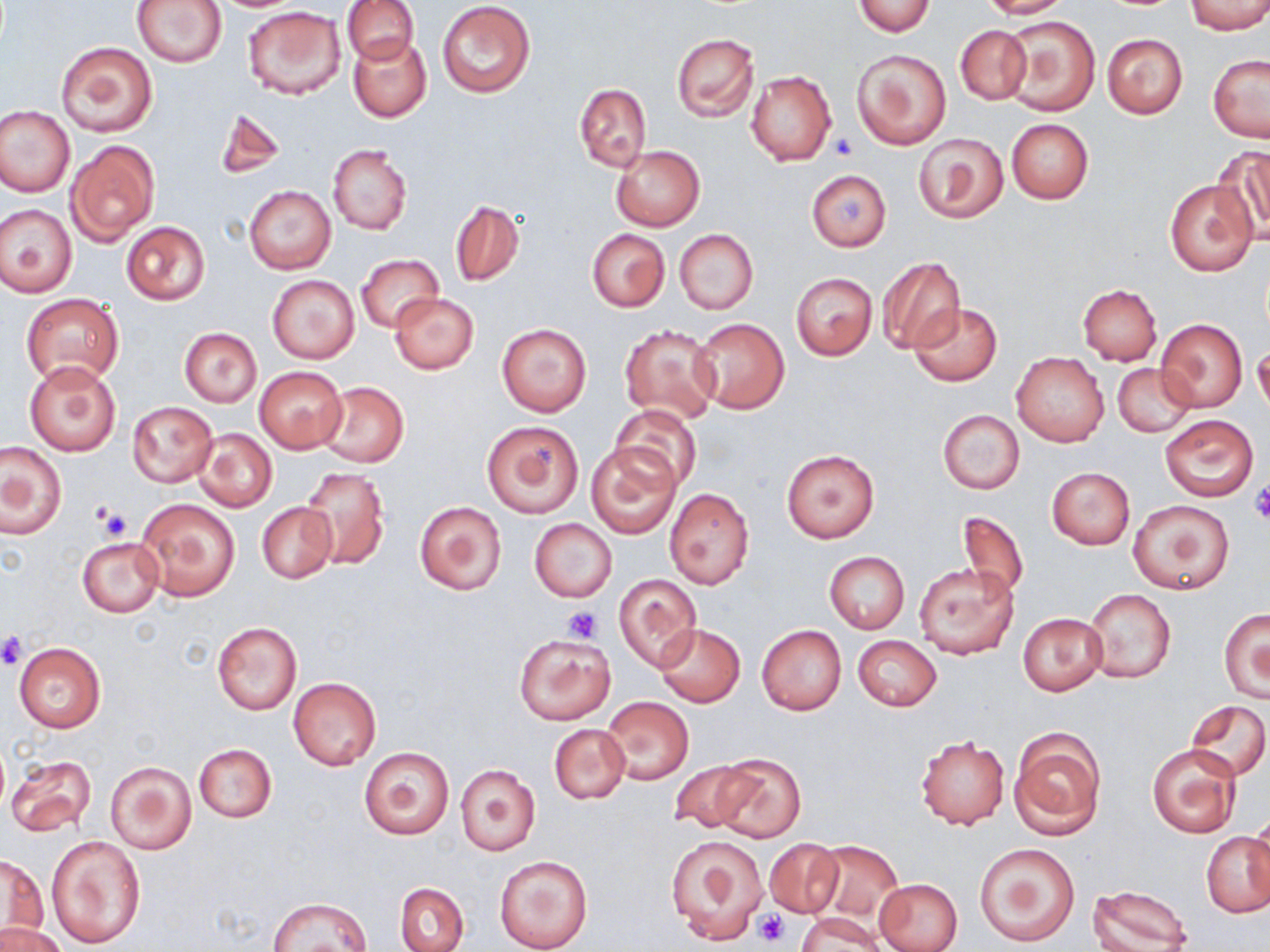 Approximate bounding boxes as [x1, y1, x2, y2] in pixels. Platelet locations: [829, 132, 859, 158], [1249, 482, 1270, 524], [94, 505, 132, 542], [562, 605, 603, 642], [0, 630, 28, 669], [754, 910, 790, 947]. Uninfected red blood cell locations: [131, 0, 228, 68], [342, 0, 419, 64], [977, 0, 1069, 18], [850, 1, 936, 36], [436, 2, 535, 97], [1185, 2, 1270, 34], [243, 7, 346, 99], [1001, 15, 1100, 117], [955, 24, 1030, 103], [672, 33, 758, 122], [1102, 33, 1187, 118], [348, 35, 432, 122], [56, 40, 158, 137], [852, 48, 950, 150], [1208, 55, 1270, 143], [746, 70, 837, 166], [574, 83, 650, 171], [216, 105, 287, 179], [0, 106, 74, 196], [1007, 118, 1093, 204], [914, 132, 1008, 224], [66, 138, 159, 244], [611, 144, 705, 231], [328, 145, 412, 234], [1217, 146, 1270, 242], [806, 169, 891, 251], [1165, 177, 1259, 277], [244, 184, 335, 275], [451, 200, 524, 286], [0, 204, 77, 296], [121, 220, 210, 305], [674, 228, 758, 314], [588, 229, 669, 312], [357, 254, 443, 334], [876, 257, 964, 353], [791, 273, 877, 359], [267, 274, 360, 365], [1078, 283, 1162, 365], [20, 292, 123, 384], [389, 292, 478, 374], [908, 302, 1003, 386], [689, 319, 788, 414], [1155, 319, 1248, 412], [496, 322, 592, 417], [619, 324, 720, 424], [180, 328, 261, 406], [1253, 345, 1270, 419], [1012, 352, 1109, 447], [24, 360, 121, 456], [1112, 363, 1196, 437], [253, 367, 347, 453], [318, 381, 410, 468], [127, 402, 218, 486], [610, 404, 701, 490], [938, 409, 1024, 494], [1161, 415, 1259, 499], [482, 420, 583, 517], [194, 428, 277, 512], [1, 442, 67, 537], [586, 442, 682, 538], [781, 449, 878, 543], [300, 467, 389, 570], [1047, 467, 1135, 548], [663, 487, 754, 588], [136, 498, 240, 601], [414, 500, 508, 596], [1128, 500, 1234, 594], [257, 501, 337, 583], [955, 511, 1028, 602], [529, 518, 617, 603], [77, 537, 165, 616], [825, 551, 909, 634], [914, 562, 1019, 661], [613, 574, 702, 670], [1084, 589, 1176, 682], [1219, 609, 1270, 703], [1018, 613, 1106, 695], [212, 621, 302, 714], [655, 624, 745, 706], [756, 624, 846, 715], [515, 634, 615, 724], [852, 635, 942, 710], [13, 641, 107, 732], [289, 678, 381, 771], [601, 696, 693, 786], [1186, 700, 1270, 782], [549, 724, 629, 802], [1007, 727, 1106, 842], [915, 735, 1009, 831], [194, 743, 276, 823], [1147, 744, 1241, 838], [358, 747, 456, 841], [5, 754, 95, 836], [711, 754, 805, 841], [666, 758, 762, 834], [104, 760, 197, 855], [455, 763, 540, 856], [1246, 816, 1270, 898], [1203, 831, 1270, 918], [665, 833, 768, 945], [46, 836, 145, 949], [765, 838, 841, 916], [811, 840, 902, 925], [974, 841, 1080, 947], [2, 855, 51, 940], [495, 855, 592, 952], [873, 878, 963, 952], [397, 883, 469, 952], [1087, 886, 1195, 952], [267, 896, 373, 950], [796, 913, 883, 952], [0, 924, 66, 952]. Slide-level diagnosis: negative for blood parasites. One field of a larger specimen. Light microscopy. Image is 1270×952 pixels. Thin blood smear. May-Grünwald-Giemsa stain. Captured at 1000x magnification.